Assess this cell for malaria.
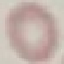
Uninfected.

stain = Giemsa
preparation = thin blood smear
image type = automatically extracted cell patch, resized to 64 × 64 pixels
capture = smartphone through the microscope eyepiece